Assess this cell for malaria.
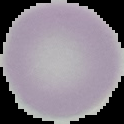

Uninfected.

Summary:
  - Image type: segmented cell region with the area outside set to black
  - Image size: 124×124 pixels
  - Preparation: thin blood film